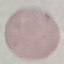

Malaria status: uninfected. Acquired by smartphone through the microscope eyepiece. Cell patch, automatically extracted from a larger field of view and resized to 64 × 64 pixels. Thin blood film. Giemsa stain.